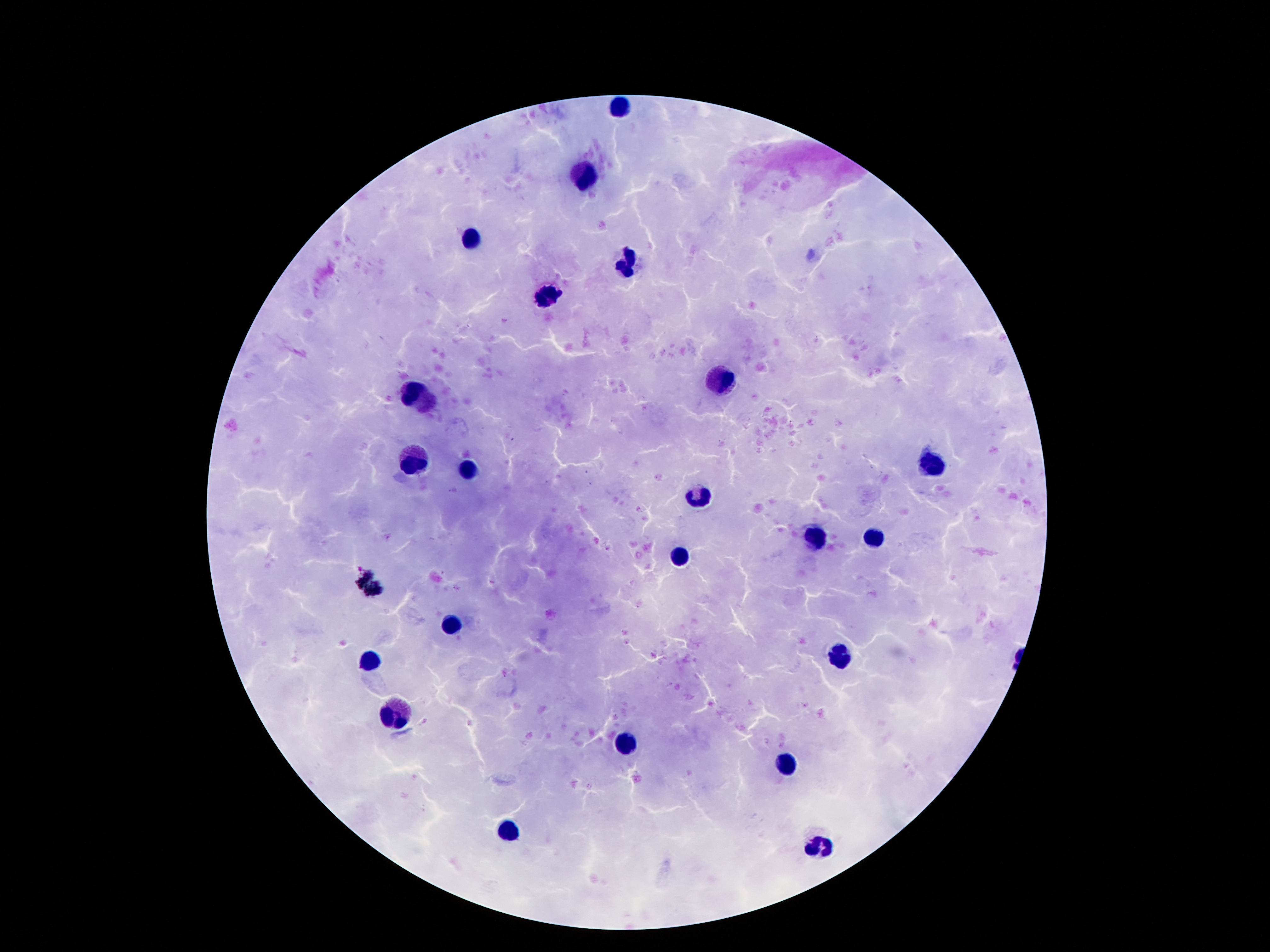

image size = 1270×952 pixels
leukocyte locations = approximate centers as (x, y) in pixels: (620, 108), (585, 177), (471, 239), (624, 265), (545, 298), (725, 382), (406, 391), (417, 460), (931, 466), (469, 471), (696, 500), (814, 539), (874, 541), (681, 558), (452, 625), (839, 659), (371, 662), (396, 713), (626, 742), (787, 762), (507, 830), (822, 847)
magnification = 100x
field of view = one from this slide
stain = Giemsa
patient malaria status = negative
capture = smartphone camera through the microscope eyepiece
preparation = thick peripheral-blood smear